Give the preparation type.
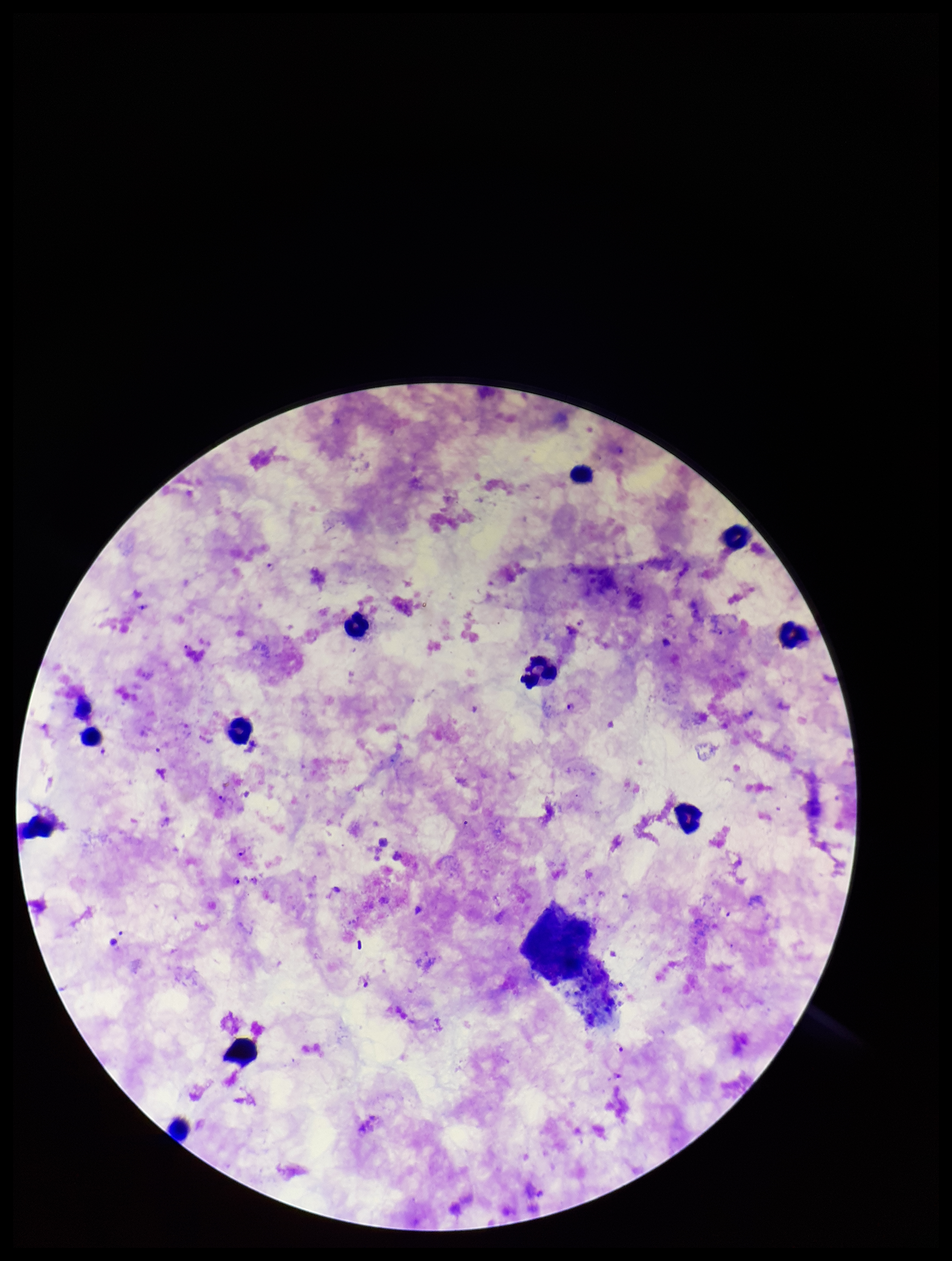
Thick.

species reported for this patient = Plasmodium falciparum
leukocyte count = 10
Plasmodium parasites = detected
stain = Giemsa
capture = smartphone photograph through the microscope eyepiece
image size = 952×1261 pixels
field of view = single
parasite count = 8
patient malaria status = infected